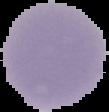
{
  "preparation": "thin blood smear",
  "image_type": "segmented cell region with the area outside set to black",
  "result": "no malaria parasites detected",
  "image_size": "109×112 pixels"
}